Locate every Plasmodium falciparum parasite and identify its life-cycle stage.
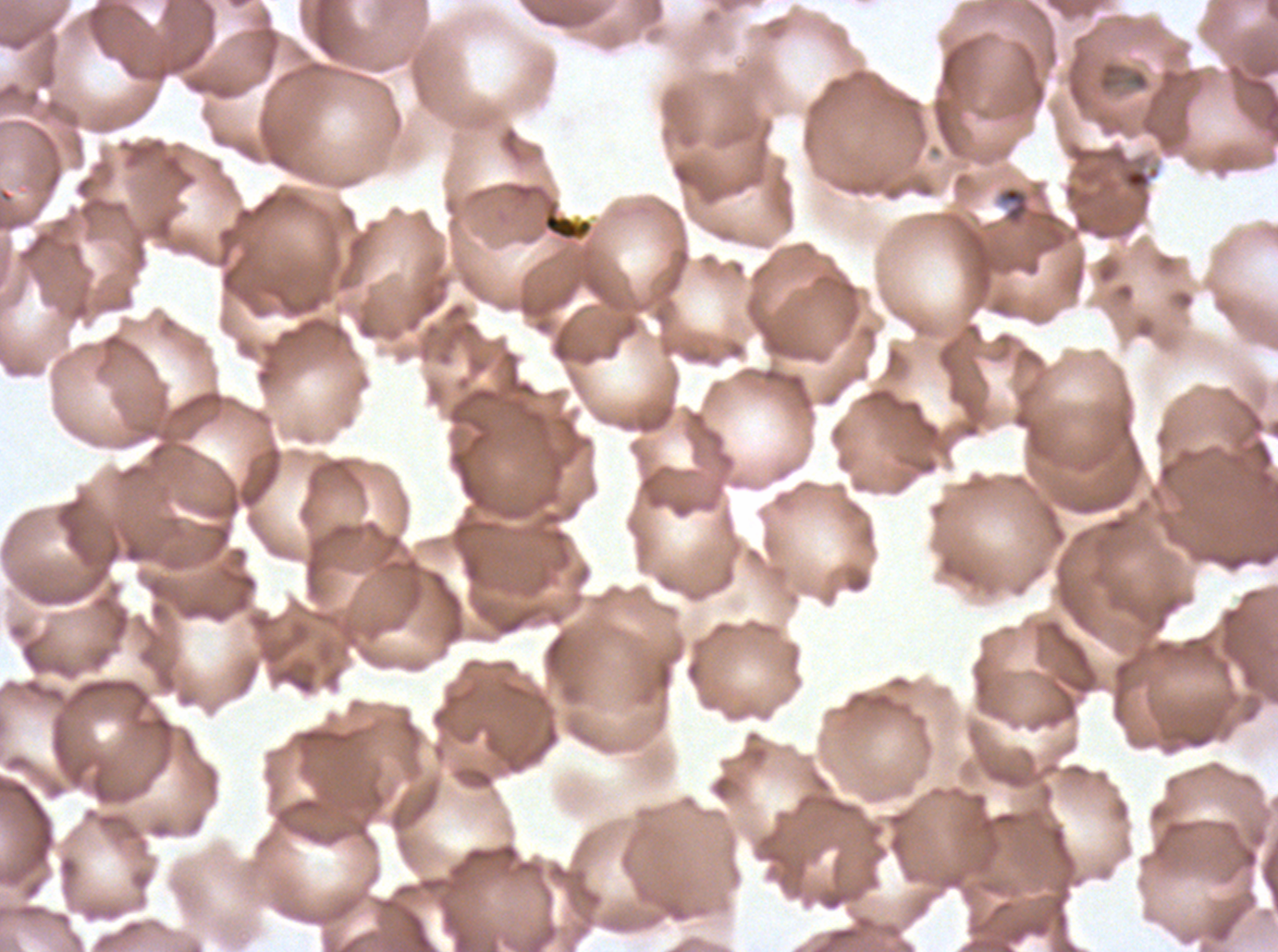
Approximate bounding boxes as [x1, y1, x2, y2] in pixels.
Rings: [997, 186, 1030, 226].
No late-ring/early-trophozoite forms, mid trophozoites, late trophozoites, early schizonts, late schizonts, segmenters, or gametocytes observed.

Summary:
  - Debris locations: [1122, 166, 1160, 191], [508, 182, 595, 242]
  - Stain: Giemsa
  - Specimen: Plasmodium falciparum from a patient in The Gambia, cultured ex vivo for 24 to 48 hours
  - Field of view: sub-image separated from a larger composite
  - Preparation: thin blood film
  - Image size: 1278×952 pixels